Assess the morphology of the erythrocytes.
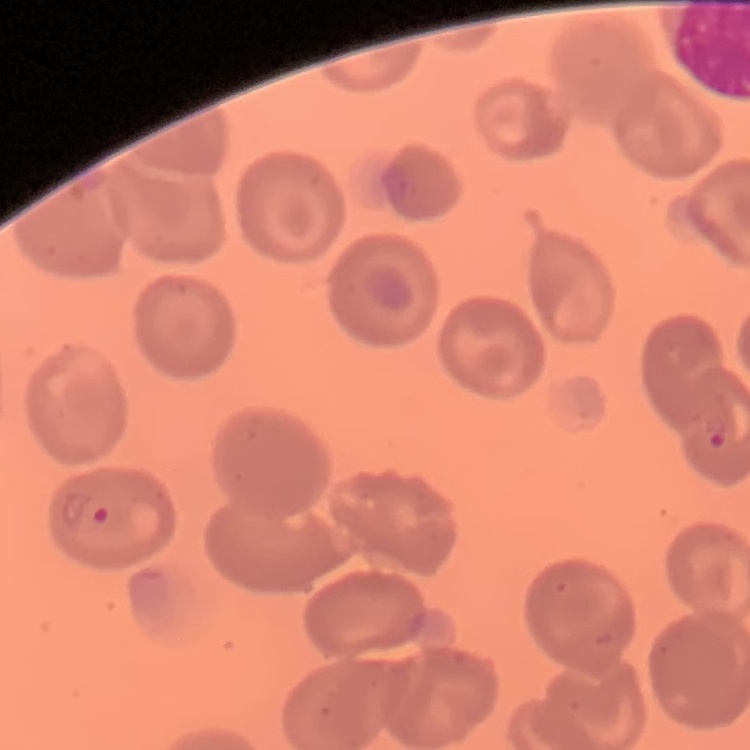

No rouleaux formation.

Square crop of a larger photomicrograph. Stained with either Field's or Giemsa. Thin blood film.